Locate every blood parasite and identify its species.
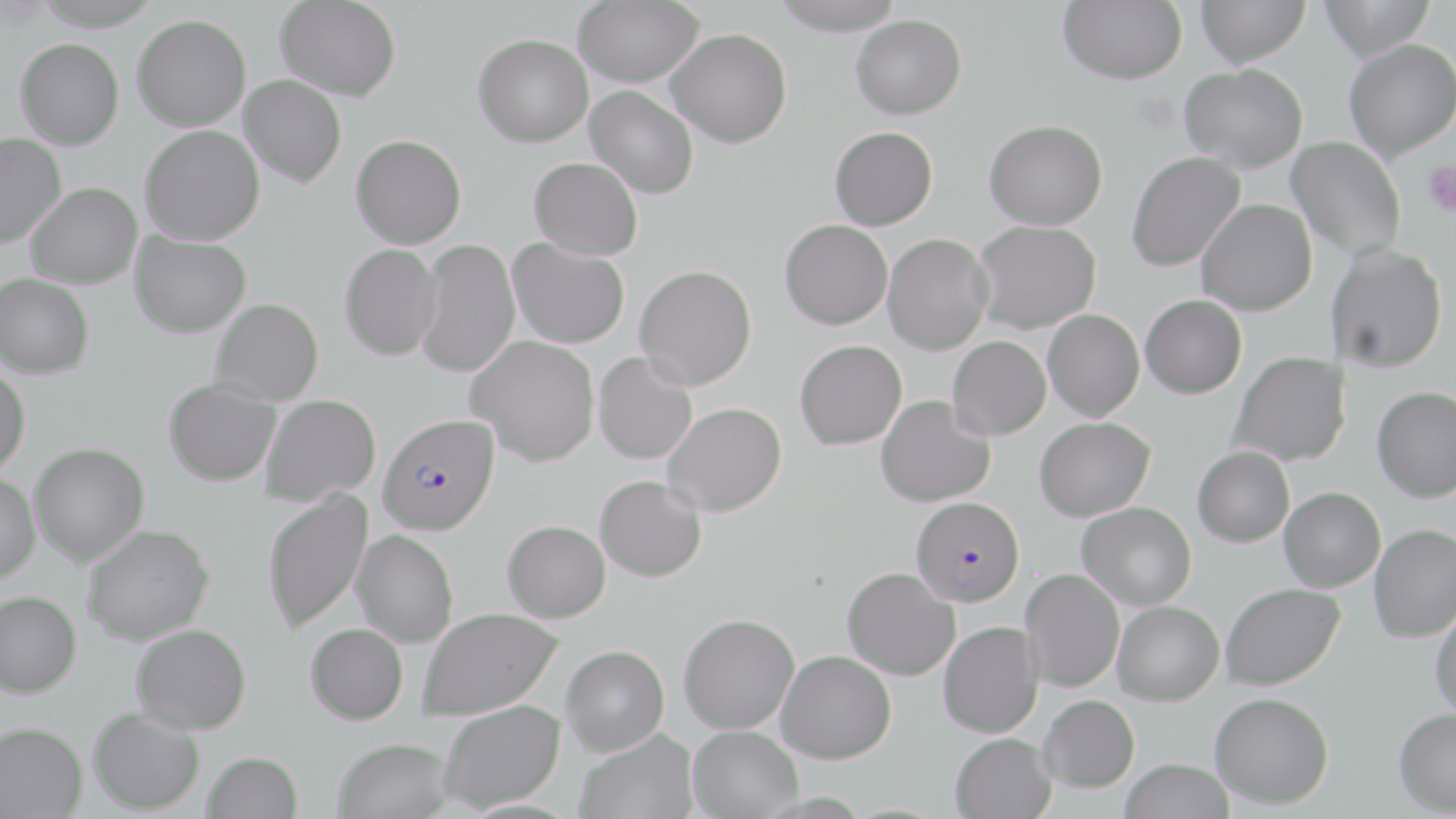
Approximate bounding boxes as (x1, y1, x2, y2) in pixels.
Plasmodium falciparum-infected red blood cells: (378, 413, 500, 535), (911, 496, 1024, 606).
No Plasmodium ovale, Plasmodium malariae, Plasmodium vivax, Babesia divergens, or Trypanosoma brucei observed.

slide-level diagnosis = Plasmodium falciparum
platelet locations = approximate bounding boxes as (x1, y1, x2, y2) in pixels: (1422, 160, 1456, 217)
modality = light microscopy
field of view = one of a larger specimen
image size = 1456×819 pixels
uninfected red blood cell locations = approximate bounding boxes as (x1, y1, x2, y2) in pixels: (30, 0, 165, 31), (274, 0, 402, 100), (573, 0, 704, 87), (769, 0, 906, 36), (1058, 0, 1187, 84), (1196, 0, 1310, 67), (1319, 0, 1437, 60), (851, 13, 967, 119), (132, 14, 251, 131), (667, 29, 792, 147), (473, 33, 593, 147), (15, 37, 124, 149), (1343, 38, 1456, 161), (1179, 63, 1308, 172), (239, 75, 347, 188), (585, 85, 699, 198), (984, 119, 1107, 230), (140, 125, 265, 245), (829, 126, 938, 230), (0, 133, 66, 248), (351, 134, 466, 248), (1287, 135, 1406, 261), (1126, 151, 1246, 272), (529, 157, 643, 260), (24, 181, 142, 288), (1196, 199, 1317, 315), (780, 219, 893, 329), (972, 220, 1101, 333), (130, 231, 251, 337), (882, 234, 993, 355), (507, 238, 629, 348), (415, 239, 521, 378), (339, 243, 442, 361), (1329, 244, 1448, 372), (635, 264, 757, 389), (0, 273, 95, 379), (1140, 294, 1247, 398), (210, 298, 324, 406), (1043, 309, 1144, 421), (467, 336, 600, 465), (947, 336, 1051, 440), (795, 339, 907, 449), (593, 351, 698, 465), (1229, 351, 1350, 466), (0, 364, 30, 477), (164, 378, 281, 486), (1372, 386, 1456, 502), (261, 394, 381, 506), (876, 396, 995, 507), (662, 402, 787, 516), (1034, 416, 1155, 521), (29, 442, 149, 566), (1192, 446, 1295, 546), (0, 472, 41, 583), (595, 475, 707, 582), (1279, 487, 1385, 592), (261, 488, 373, 635), (1077, 502, 1196, 609), (502, 520, 610, 622), (81, 523, 214, 645), (1369, 524, 1456, 642), (353, 530, 458, 647), (842, 567, 960, 680), (1020, 569, 1124, 692), (1220, 583, 1344, 690), (0, 590, 81, 698), (1112, 601, 1224, 705), (1430, 603, 1456, 719), (419, 607, 564, 719), (678, 613, 800, 733), (938, 622, 1043, 738), (130, 623, 251, 734), (305, 623, 408, 725), (561, 645, 669, 755), (776, 650, 896, 763), (1209, 691, 1334, 808), (1038, 695, 1139, 793), (438, 700, 565, 811), (1393, 707, 1456, 815), (88, 708, 204, 814), (0, 721, 87, 819), (687, 725, 803, 818), (574, 729, 698, 819), (950, 733, 1057, 819), (333, 737, 455, 819), (202, 751, 303, 819), (1120, 758, 1234, 819)
preparation = thin blood film
magnification = 1000x
stain = May-Grünwald-Giemsa